Report the malaria status of this cell.
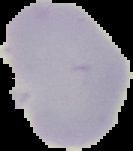
It is uninfected.

image size = 133×151 pixels
image type = cell region segmented out of the field of view; surrounding area masked to black
preparation = thin blood smear